Comment on the morphology of the erythrocytes.
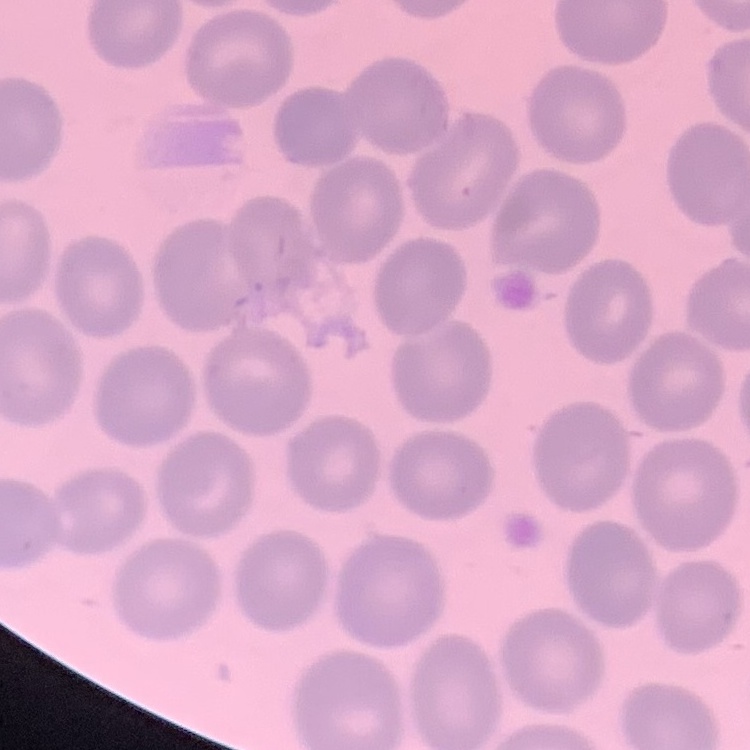
No rouleaux formation.

{
  "preparation": "thin peripheral smear",
  "image_type": "square crop of a larger photomicrograph",
  "stain": "Field's or Giemsa"
}